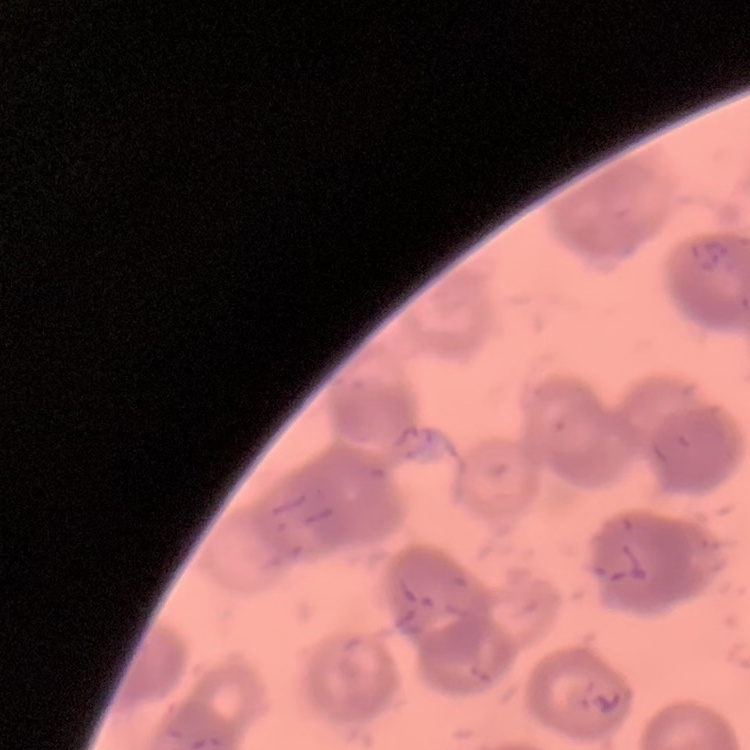
red blood cell morphology = rouleaux formation
image type = square crop of a larger photomicrograph
stain = Field's or Giemsa
preparation = thin peripheral smear